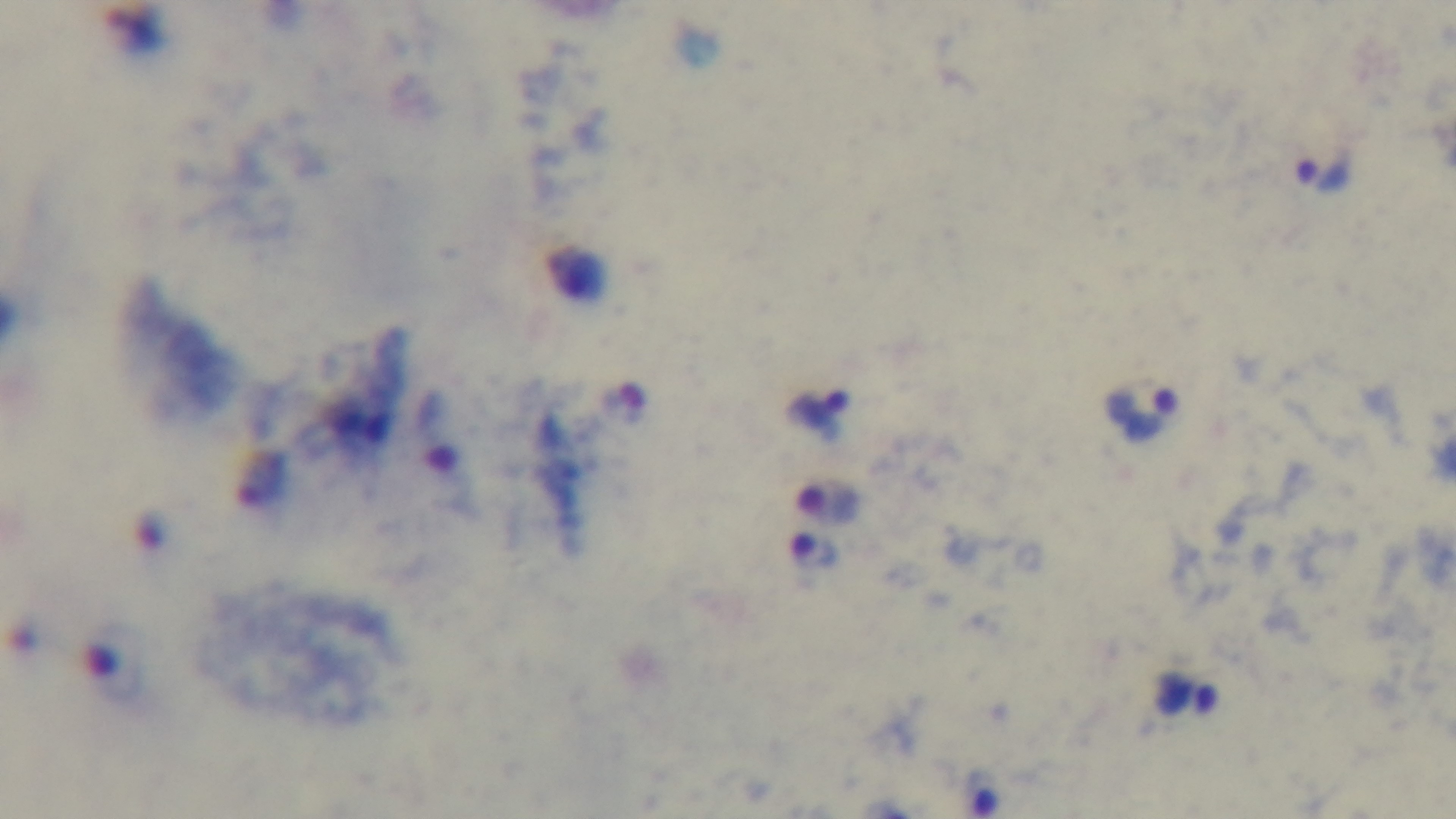

100x oil-immersion objective. Malaria status: infected. Giemsa-stained. Photomicrograph. Single field of view. Preparation: thick smear. Mounted 4K digital camera.